Assess the morphology of the erythrocytes.
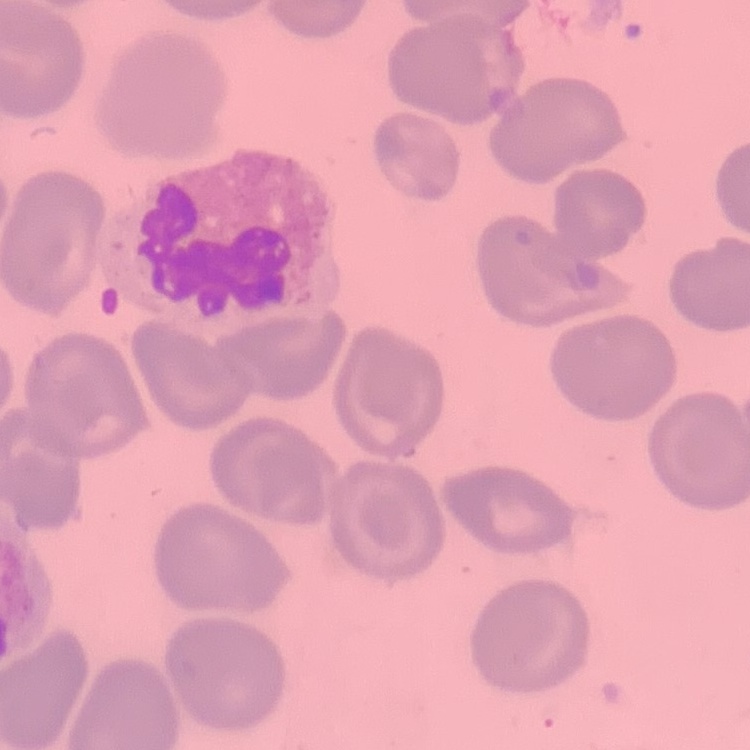
No rouleaux formation.

Square crop of a larger photomicrograph. Stained with either Field's or Giemsa. Thin peripheral smear.